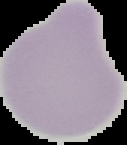
result = no malaria parasites detected
preparation = thin blood film
image size = 127×145 pixels
image type = segmented cell region on a black background